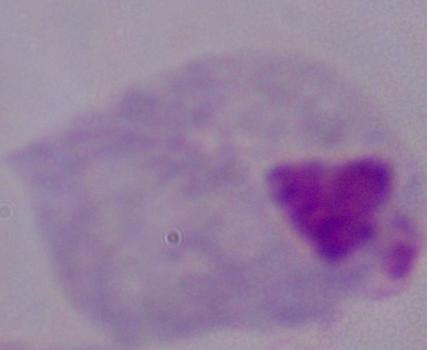
modality = micrograph
magnification = 1000x
identification = trichomonad